Outline each blood parasite and name the species.
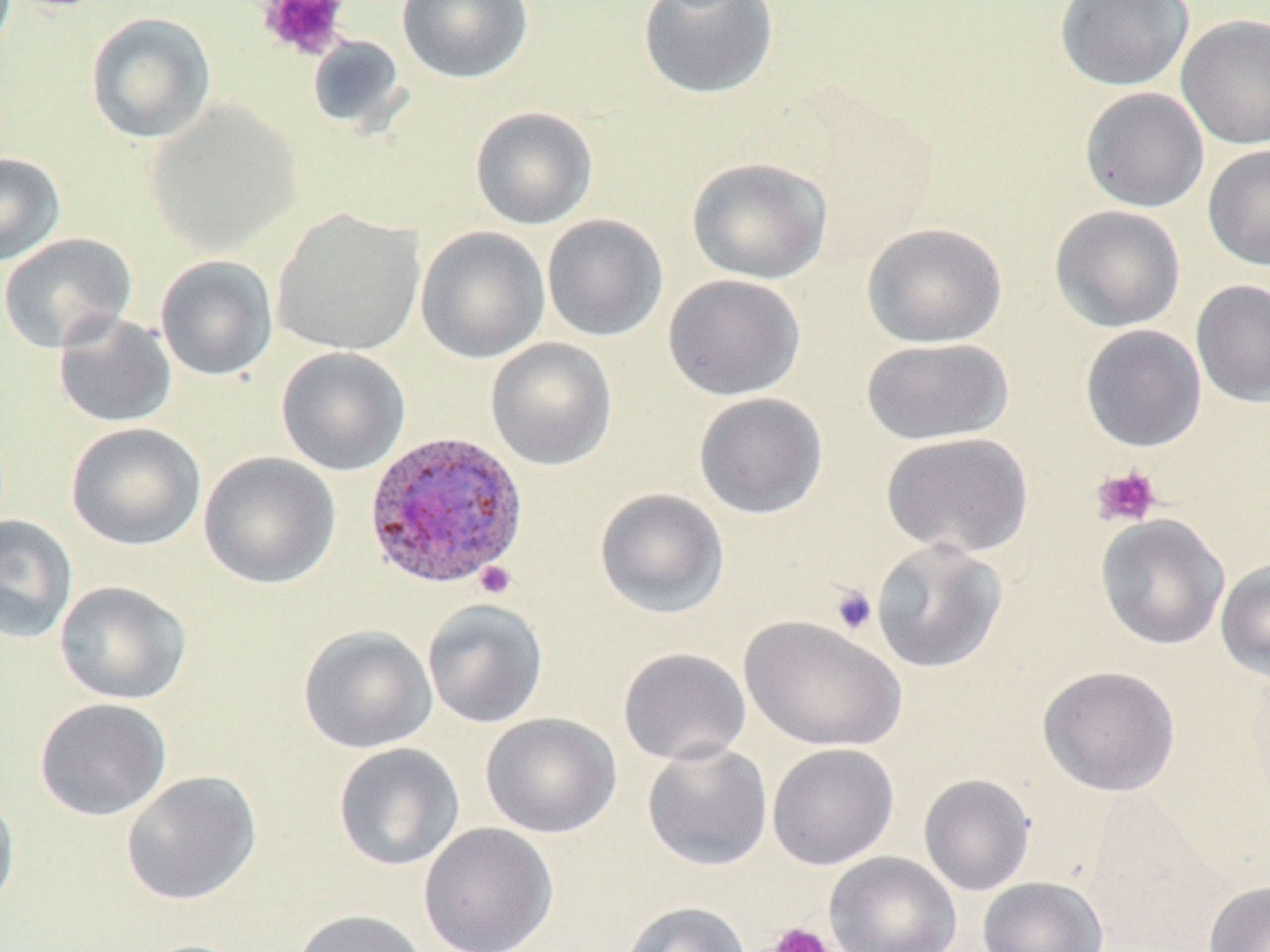

Approximate bounding boxes as [x1, y1, x2, y2] in pixels.
Plasmodium ovale-infected red blood cells: [363, 430, 529, 591].
No Plasmodium falciparum, Plasmodium malariae, Plasmodium vivax, Babesia divergens, or Trypanosoma brucei observed.

{
  "slide_level_diagnosis": "Plasmodium ovale",
  "image_size": "1270×952 pixels",
  "modality": "optical microscopy",
  "uninfected_red_blood_cell_locations_subset": "approximate bounding boxes as [x1, y1, x2, y2] in pixels: [396, 0, 534, 84], [637, 0, 780, 100], [1054, 0, 1194, 92], [85, 12, 217, 144], [1176, 13, 1270, 150], [306, 34, 409, 135], [1079, 86, 1209, 213], [145, 101, 302, 256], [469, 106, 599, 230], [1202, 143, 1270, 271], [0, 152, 66, 267], [686, 156, 833, 284], [1049, 204, 1186, 333], [271, 208, 425, 357], [542, 214, 669, 342], [861, 222, 1008, 348], [415, 226, 550, 364], [0, 232, 137, 354], [154, 255, 278, 381], [662, 273, 807, 401], [1190, 279, 1270, 407], [52, 312, 178, 429], [1079, 325, 1207, 453], [485, 337, 618, 471], [860, 337, 1014, 446], [275, 347, 411, 476], [693, 392, 828, 519], [65, 422, 206, 551], [880, 432, 1034, 558], [198, 451, 341, 590], [593, 487, 730, 619], [0, 514, 78, 644], [1096, 514, 1230, 651], [870, 539, 1008, 674], [1215, 559, 1270, 682], [53, 580, 192, 705], [422, 598, 549, 729], [738, 614, 907, 752], [298, 624, 438, 754], [618, 647, 752, 766], [1037, 665, 1181, 797], [34, 697, 172, 821], [481, 712, 621, 839], [641, 740, 773, 871], [332, 742, 465, 872], [766, 743, 899, 870], [120, 771, 262, 906], [918, 774, 1035, 896], [0, 788, 21, 919], [1081, 789, 1223, 947], [418, 823, 559, 952], [825, 851, 962, 952], [977, 876, 1109, 952], [1203, 880, 1270, 952], [621, 901, 751, 952], [291, 908, 432, 952]",
  "magnification": "1000x",
  "platelet_locations_subset": "approximate bounding boxes as [x1, y1, x2, y2] in pixels: [1090, 465, 1162, 528], [474, 561, 517, 599], [829, 584, 878, 636], [764, 922, 837, 952]",
  "preparation": "thin blood smear",
  "stain": "May-Grünwald-Giemsa",
  "field_of_view": "single"
}